Identify the blood parasite species.
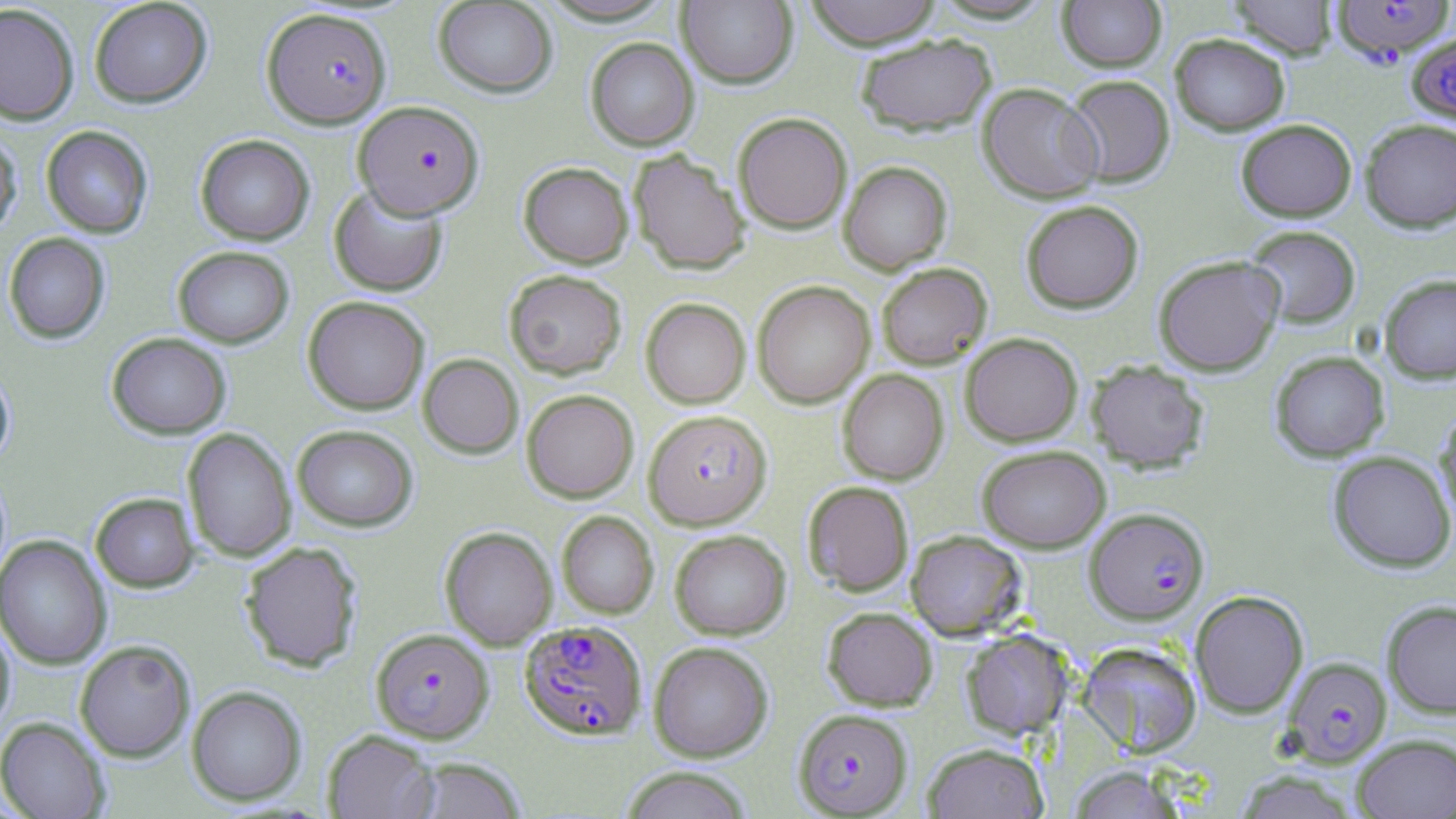

Plasmodium falciparum.

Approximate bounding boxes as (x1,y1)-(x2,y2) corner pairs in pixels. Uninfected red blood cell locations: (88,0)-(212,108), (536,0)-(679,26), (803,0)-(943,49), (1057,0)-(1167,72), (1228,0)-(1338,59), (433,1)-(558,97), (677,1)-(798,88), (0,3)-(80,126), (854,33)-(996,136), (1170,33)-(1290,135), (585,37)-(699,150), (1064,75)-(1175,187), (978,82)-(1103,203), (733,112)-(852,233), (1360,118)-(1456,232), (1236,119)-(1357,221), (40,125)-(154,238), (0,131)-(22,240), (195,134)-(315,245), (628,149)-(750,275), (518,161)-(633,268), (838,161)-(952,275), (328,185)-(448,296), (1020,200)-(1144,313), (1243,224)-(1361,329), (3,232)-(110,344), (172,246)-(294,347), (1153,255)-(1285,376), (876,263)-(992,369), (504,269)-(627,379), (1379,274)-(1456,383), (752,281)-(875,408), (302,296)-(430,415), (640,297)-(751,408), (106,332)-(231,439), (960,333)-(1082,446), (1270,351)-(1389,462), (418,353)-(523,458), (1085,360)-(1211,473), (0,367)-(15,468), (837,370)-(949,485), (522,389)-(639,503), (1434,406)-(1456,531), (292,424)-(418,531), (182,427)-(296,563), (976,444)-(1111,552), (1328,451)-(1455,572), (803,480)-(914,596), (90,492)-(199,592), (556,511)-(658,619), (440,526)-(557,650), (670,529)-(790,640), (906,529)-(1027,640), (0,535)-(112,670), (239,540)-(363,672), (1189,590)-(1309,718), (1381,599)-(1456,718), (822,606)-(938,711), (0,619)-(15,733), (961,629)-(1073,739), (75,640)-(195,762), (649,641)-(774,762), (1077,641)-(1203,758), (186,685)-(307,806), (0,717)-(110,819), (323,730)-(439,818), (1352,733)-(1456,818), (922,742)-(1048,819), (409,757)-(528,819), (1067,766)-(1187,818), (620,767)-(753,819), (1235,771)-(1359,819). Plasmodium falciparum-infected red blood cell locations: (1332,0)-(1453,63), (261,7)-(391,128), (1407,33)-(1456,125), (353,101)-(484,219), (647,412)-(774,532), (1085,508)-(1209,624), (518,620)-(646,741), (370,627)-(494,744), (1283,656)-(1392,765), (793,708)-(913,817). May-Grünwald-Giemsa-stained preparation. Captured at 1000x magnification. One field of a larger specimen. Image is 1456×819 pixels. Thin blood smear. Light microscopy.